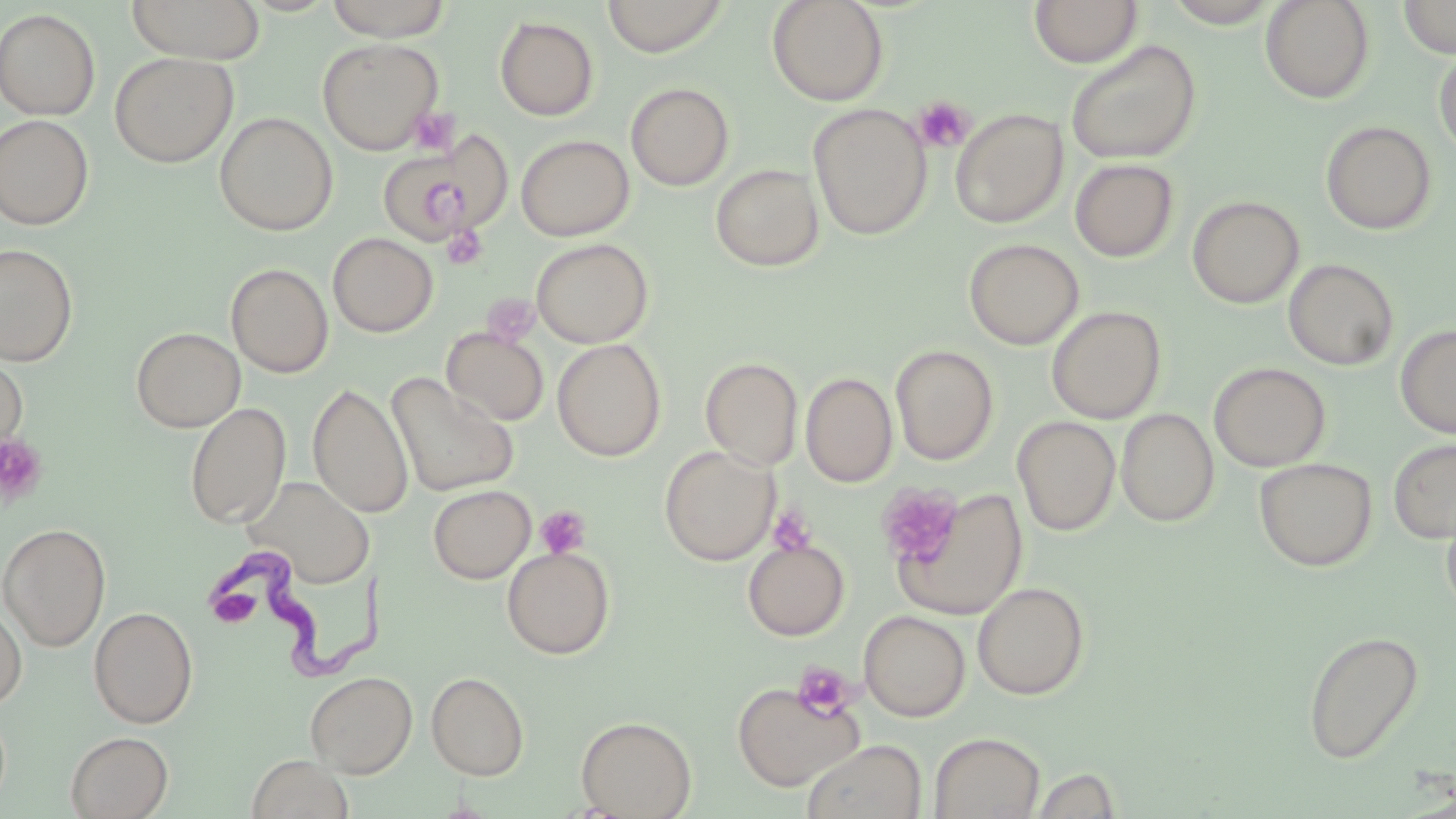 Approximate bounding boxes as (x1, y1, x2, y2) in pixels. Trypanosoma brucei locations: (204, 550, 406, 683). Uninfected red blood cell locations: (125, 0, 265, 64), (324, 0, 453, 42), (602, 0, 729, 57), (766, 0, 889, 106), (1162, 0, 1282, 27), (1260, 0, 1374, 103), (1398, 0, 1456, 58), (1029, 1, 1142, 67), (0, 8, 101, 120), (495, 16, 598, 120), (317, 37, 443, 155), (1065, 39, 1201, 165), (1433, 47, 1456, 159), (109, 52, 238, 167), (625, 82, 734, 191), (808, 103, 931, 240), (950, 108, 1067, 228), (214, 111, 338, 236), (0, 114, 94, 230), (1320, 121, 1437, 235), (375, 134, 510, 247), (516, 134, 635, 241), (1070, 159, 1179, 262), (710, 163, 824, 272), (1187, 196, 1304, 309), (328, 233, 438, 337), (531, 238, 653, 348), (964, 238, 1084, 350), (0, 243, 78, 367), (1283, 259, 1399, 370), (226, 262, 333, 377), (1047, 305, 1166, 423), (1395, 324, 1456, 439), (131, 327, 245, 432), (442, 328, 549, 426), (439, 333, 666, 445), (552, 339, 666, 462), (890, 344, 998, 464), (0, 351, 28, 457), (700, 357, 803, 469), (1209, 362, 1330, 471), (801, 372, 897, 487), (386, 374, 520, 497), (307, 382, 414, 517), (186, 402, 291, 528), (1116, 408, 1219, 527), (1012, 417, 1120, 536), (1388, 438, 1456, 543), (659, 445, 779, 565), (1254, 457, 1378, 571), (245, 476, 376, 588), (873, 481, 966, 579), (428, 484, 536, 584), (887, 485, 1028, 621), (1441, 498, 1456, 618), (0, 523, 111, 651), (742, 539, 850, 641), (502, 547, 615, 659), (972, 581, 1090, 700), (0, 600, 27, 709), (88, 606, 198, 728), (859, 610, 970, 721), (1303, 630, 1424, 764), (305, 671, 417, 777), (426, 671, 529, 780), (731, 679, 864, 791), (575, 715, 697, 818), (65, 731, 173, 818), (929, 732, 1045, 819), (801, 739, 927, 819), (246, 754, 354, 819), (1031, 767, 1122, 818). Platelet locations: (913, 96, 974, 152), (408, 107, 460, 156), (445, 226, 488, 269), (0, 434, 49, 507), (876, 484, 963, 569), (536, 506, 591, 558), (768, 507, 817, 554), (213, 592, 265, 633), (791, 661, 857, 722). Slide-level diagnosis: Trypanosoma brucei. Thin blood smear. May-Grünwald-Giemsa-stained preparation. One field of a larger specimen. Light microscopy. Image is 1456×819 pixels. 1000x magnification.